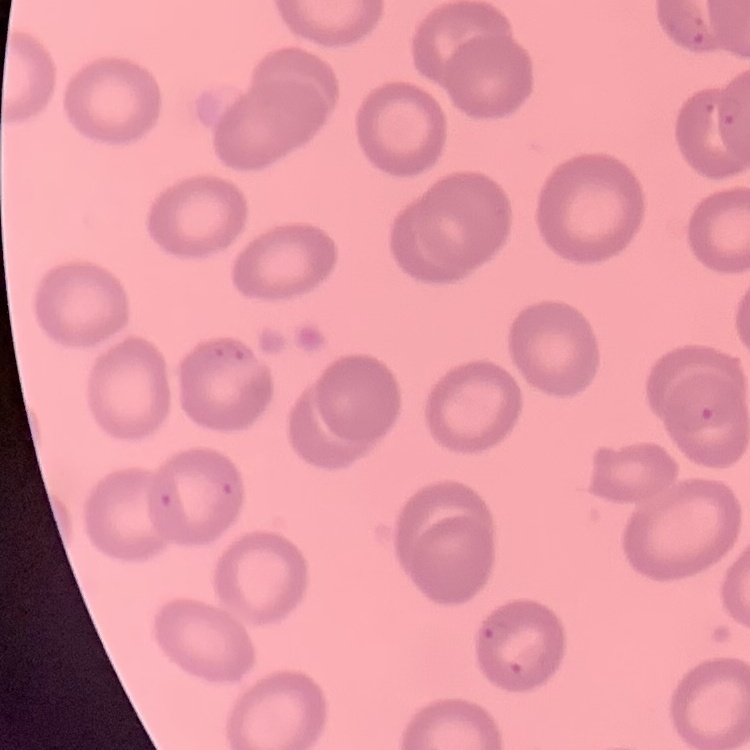

erythrocyte morphology = no rouleaux formation
stain = Field's or Giemsa
image type = square crop of a larger photomicrograph
preparation = thin peripheral smear